Comment on the morphology of the red blood cells.
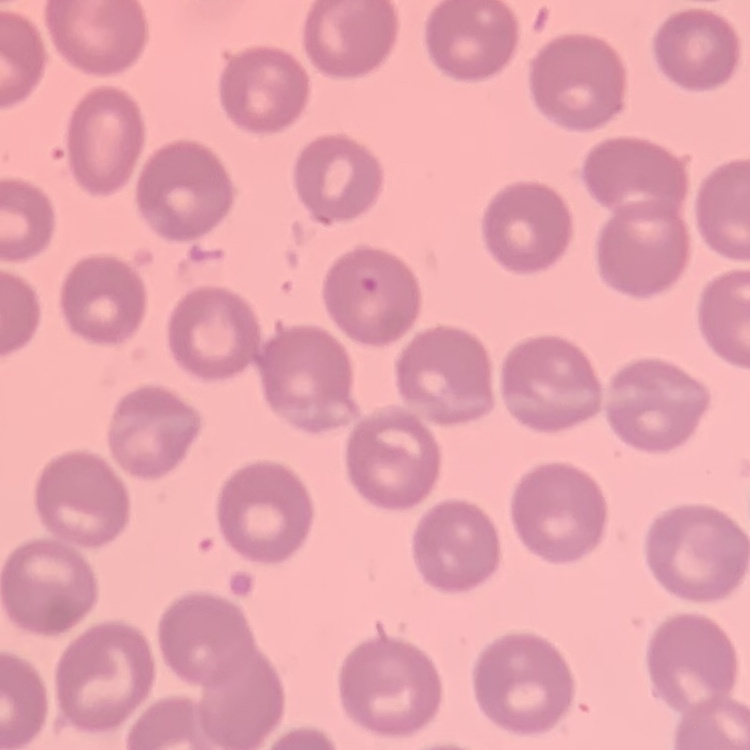

They show no rouleaux formation.

Summary:
  - Preparation: thin peripheral smear
  - Image type: square crop of a larger photomicrograph
  - Stain: Field's or Giemsa